Report the malaria status of this cell.
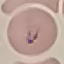

Parasitized.

Summary:
  - Image type: cell patch, automatically extracted from a larger field of view and resized to 64 × 64 pixels
  - Preparation: thin smear
  - Stain: Giemsa
  - Capture: smartphone camera at the microscope eyepiece